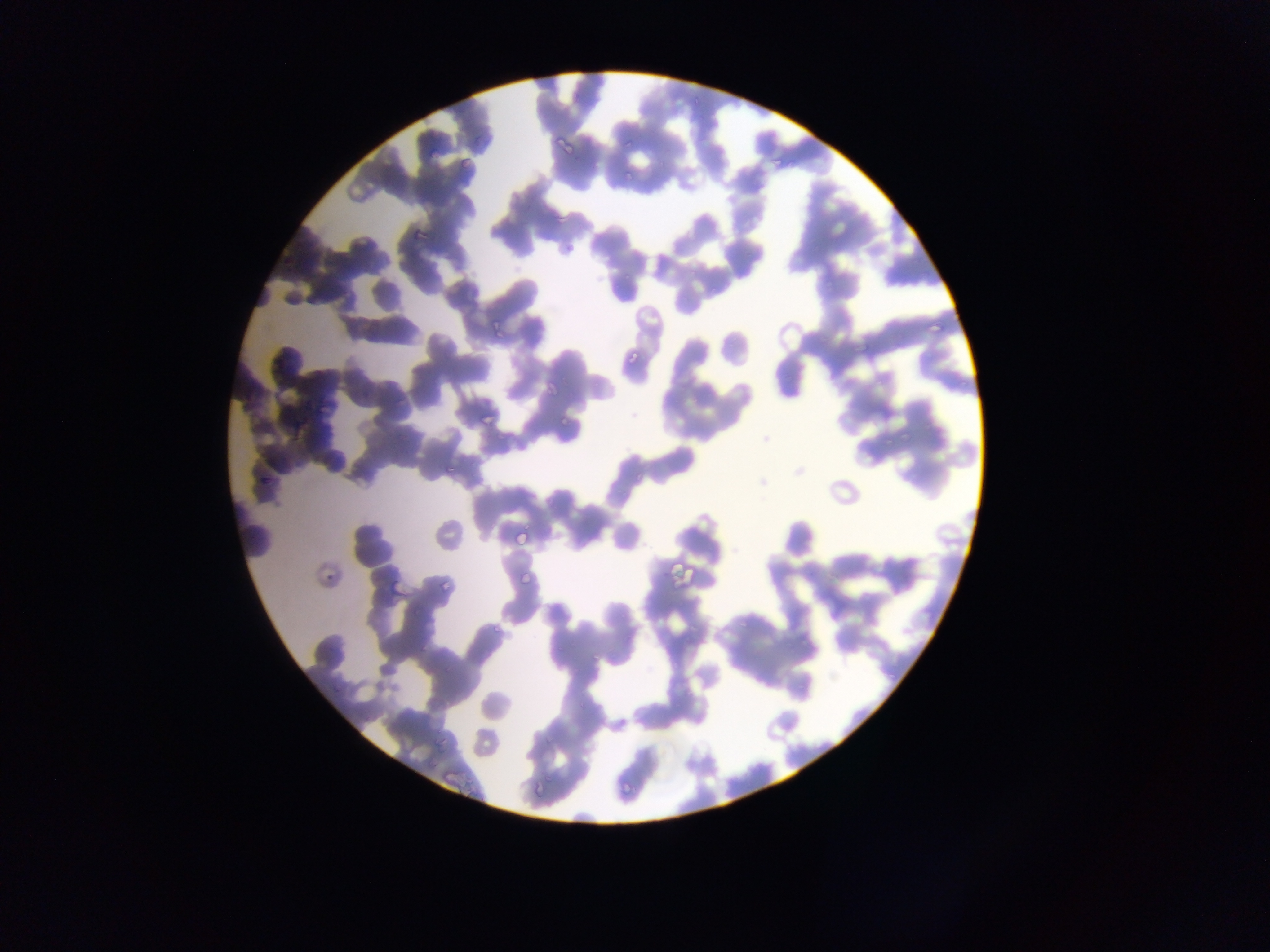
Approximate bounding boxes as (left, top, right, bottom) in pixels. Plasmodium parasite locations: (622, 133, 642, 148), (554, 136, 574, 152), (458, 154, 479, 172), (771, 159, 781, 168), (622, 168, 635, 182), (548, 205, 568, 224), (413, 228, 428, 243), (711, 280, 727, 295), (925, 314, 945, 331), (490, 320, 505, 334), (627, 345, 644, 367), (541, 381, 560, 402), (479, 406, 496, 424), (559, 415, 571, 427), (900, 429, 910, 442), (440, 460, 458, 478), (259, 472, 271, 493), (510, 524, 530, 546), (316, 558, 340, 585), (520, 565, 532, 589), (392, 571, 413, 603), (492, 617, 505, 638), (589, 647, 602, 665), (576, 701, 587, 712), (431, 727, 448, 753), (533, 772, 550, 791), (620, 773, 633, 797), (529, 779, 547, 799). One field of view. Thin blood film. Sample from Ghana. Mobile-phone photograph taken through the microscope. Image is 1270×952 pixels.